Name the blood parasite species.
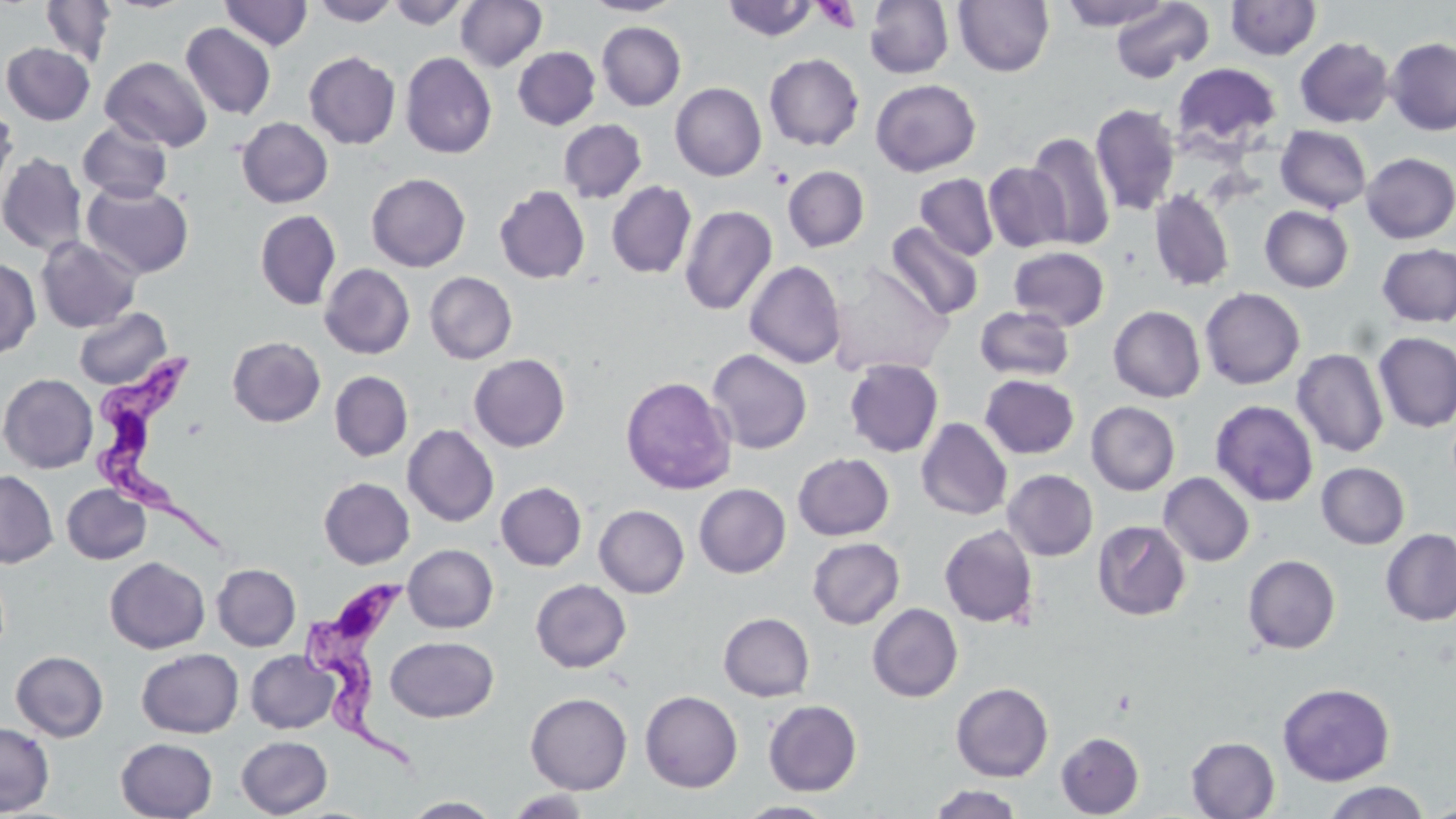

Trypanosoma brucei.

modality = optical microscopy
stain = May-Grünwald-Giemsa
preparation = thin blood film
image size = 1456×819 pixels
field of view = one of a larger specimen
magnification = 1000x
Trypanosoma brucei locations = approximate bounding boxes as (x1,y1)-(x2,y2) corner pairs in pixels: (90,347)-(229,556), (302,580)-(425,774)
platelet locations = approximate bounding boxes as (x1,y1)-(x2,y2) corner pairs in pixels: (813,1)-(861,33)
uninfected red blood cell locations = approximate bounding boxes as (x1,y1)-(x2,y2) corner pairs in pixels: (39,0)-(115,67), (311,0)-(400,26), (386,0)-(471,29), (455,0)-(547,72), (582,0)-(682,16), (864,0)-(954,78), (953,0)-(1054,76), (1061,0)-(1171,30), (1225,0)-(1322,60), (219,1)-(313,51), (721,1)-(819,41), (1109,1)-(1215,83), (597,22)-(686,111), (181,23)-(276,119), (1295,37)-(1394,128), (1385,38)-(1456,135), (1,43)-(95,125), (512,47)-(600,130), (304,51)-(401,149), (401,52)-(497,159), (764,53)-(864,151), (100,56)-(213,152), (1172,62)-(1281,152), (870,79)-(981,176), (670,82)-(767,181), (0,102)-(18,197), (1090,104)-(1181,217), (237,117)-(333,207), (558,119)-(647,203), (78,120)-(173,202), (1275,125)-(1372,214), (1026,132)-(1116,250), (0,152)-(87,255), (1361,153)-(1456,243), (983,162)-(1071,252), (783,166)-(870,252), (366,173)-(471,272), (915,174)-(999,261), (607,181)-(697,279), (82,182)-(194,278), (495,185)-(590,283), (1149,189)-(1235,292), (679,204)-(777,316), (1260,206)-(1353,292), (255,210)-(341,310), (884,223)-(984,321), (36,236)-(142,333), (1377,243)-(1456,327), (1009,246)-(1109,330), (0,258)-(40,359), (827,260)-(955,378), (744,261)-(846,368), (320,263)-(415,359), (425,271)-(518,364), (1200,287)-(1305,390), (1108,305)-(1205,402), (975,306)-(1074,381), (74,307)-(171,390), (1373,332)-(1456,433), (228,336)-(325,427), (1292,348)-(1389,457), (706,349)-(812,454), (469,354)-(570,452), (844,358)-(944,457), (330,371)-(413,461), (0,373)-(99,473), (979,374)-(1080,459), (621,376)-(737,494), (1210,399)-(1319,507), (1086,401)-(1180,495), (916,418)-(1012,520), (402,424)-(498,527), (793,453)-(894,540), (1316,462)-(1409,549), (0,469)-(58,568), (1003,469)-(1098,561), (1158,472)-(1254,566), (319,477)-(415,569), (496,482)-(586,571), (693,483)-(791,578), (62,484)-(151,564), (594,505)-(689,598), (1093,520)-(1191,620), (939,525)-(1038,628), (1380,528)-(1456,626), (807,537)-(905,629), (403,544)-(498,633), (1243,554)-(1340,654), (105,556)-(209,654), (212,563)-(301,651), (530,579)-(631,672), (867,603)-(963,702), (719,612)-(815,701), (385,636)-(498,722), (137,648)-(243,738), (245,650)-(340,733), (11,651)-(108,742), (951,682)-(1053,782), (1278,683)-(1394,785), (640,690)-(743,792), (525,692)-(632,795), (763,700)-(862,796), (0,721)-(54,816), (1056,732)-(1144,818), (236,735)-(333,817), (1186,737)-(1280,818), (115,738)-(218,819), (1322,781)-(1431,819), (927,784)-(1023,818), (506,789)-(592,817), (402,796)-(502,818), (735,801)-(839,818)